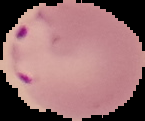
image_type: segmented cell region on a black background
preparation: thin blood film
image_size: 145×121 pixels
result: malaria parasites identified